Assess this cell for malaria.
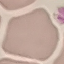

Uninfected.

Summary:
  - Image type: cell patch, automatically extracted from a larger field of view and resized to 64 × 64 pixels
  - Capture: smartphone through the microscope eyepiece
  - Preparation: thin blood smear
  - Stain: Giemsa